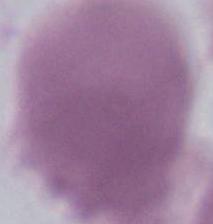

{
  "modality": "photomicrograph",
  "magnification": "1000x",
  "identification": "red blood cell"
}